Mark where platelets are.
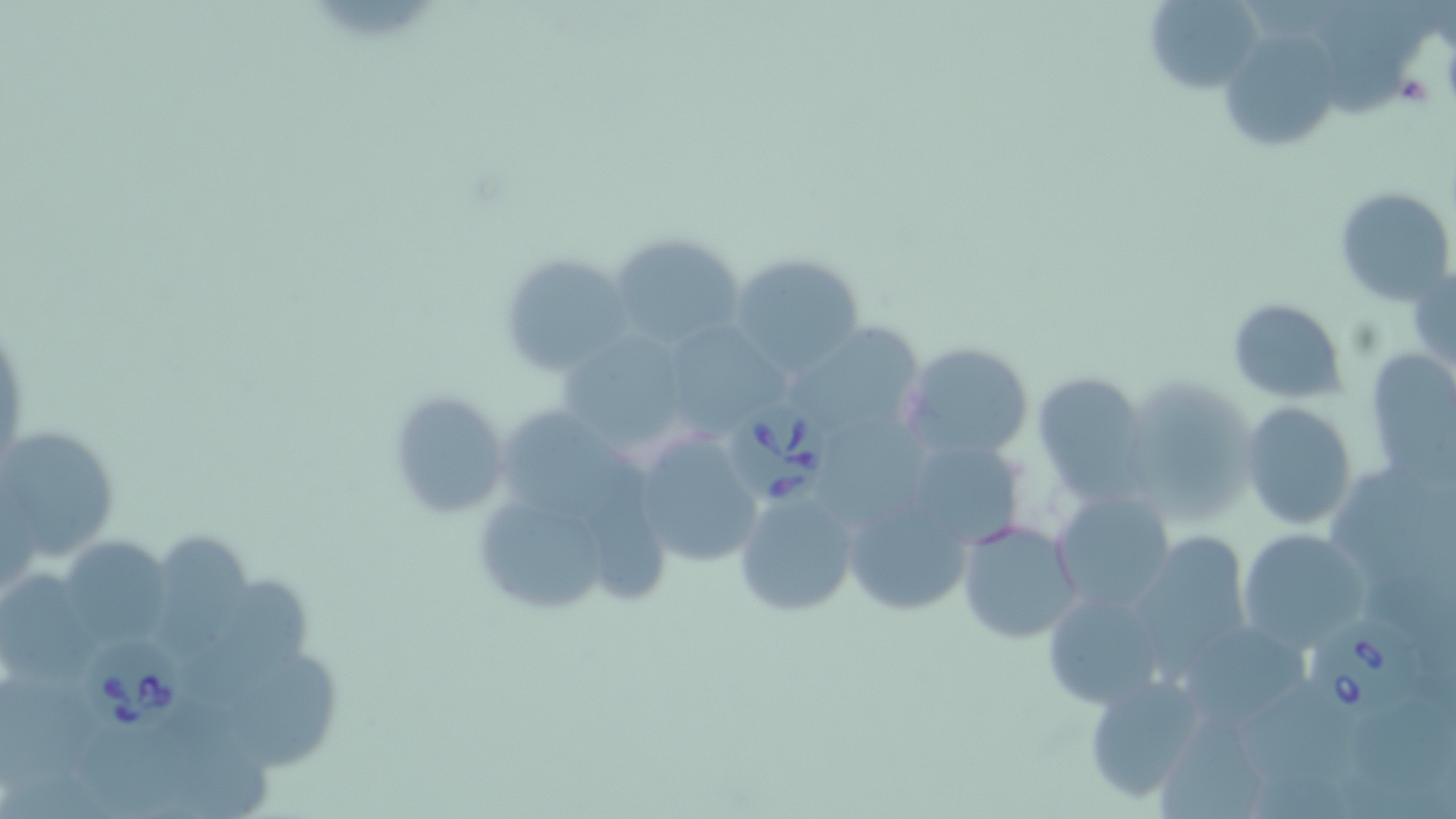
Approximate bounding boxes as [x1, y1, x2, y2] in pixels.
Platelets: [1395, 72, 1436, 107].

Uninfected red blood cell locations: [1141, 0, 1266, 93], [1318, 15, 1407, 117], [1225, 27, 1342, 151], [1334, 186, 1455, 307], [609, 231, 749, 350], [501, 249, 630, 375], [728, 253, 864, 375], [1407, 262, 1456, 375], [1227, 298, 1348, 402], [794, 328, 930, 428], [669, 329, 794, 436], [562, 332, 687, 452], [901, 342, 1035, 461], [1373, 351, 1456, 495], [1032, 370, 1152, 499], [1119, 375, 1258, 528], [388, 391, 510, 521], [490, 400, 646, 523], [1239, 401, 1359, 531], [826, 415, 930, 526], [631, 425, 769, 572], [1, 426, 119, 564], [922, 447, 1019, 546], [1328, 465, 1451, 578], [594, 476, 665, 605], [733, 486, 860, 619], [482, 490, 613, 615], [1050, 490, 1176, 611], [842, 492, 975, 621], [956, 519, 1083, 645], [1238, 528, 1371, 651], [150, 530, 254, 668], [1131, 532, 1252, 672], [64, 534, 169, 643], [0, 573, 98, 682], [190, 580, 309, 705], [1042, 587, 1167, 704], [1174, 616, 1316, 735], [227, 655, 340, 769], [1083, 672, 1209, 806], [0, 679, 97, 786], [1247, 679, 1371, 776], [1349, 706, 1456, 795], [1150, 720, 1270, 819], [160, 722, 270, 819], [82, 729, 185, 816]. Babesia divergens-infected red blood cell locations: [730, 398, 831, 502], [1308, 615, 1419, 716], [79, 631, 194, 742]. Slide-level diagnosis: Babesia divergens. Optical microscopy. Single field of view. Thin blood film. Image is 1456×819 pixels. 1000x magnification. May-Grünwald-Giemsa-stained preparation.